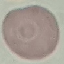
{
  "result": "negative for malaria parasites",
  "image_type": "cell patch, automatically extracted from a larger field of view and resized to 64 × 64 pixels",
  "stain": "Giemsa",
  "preparation": "thin blood film",
  "capture": "smartphone camera at the microscope eyepiece"
}